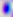 Captured at 400x magnification. Photomicrograph. Toxoplasma gondii is shown.